Name the blood parasite species.
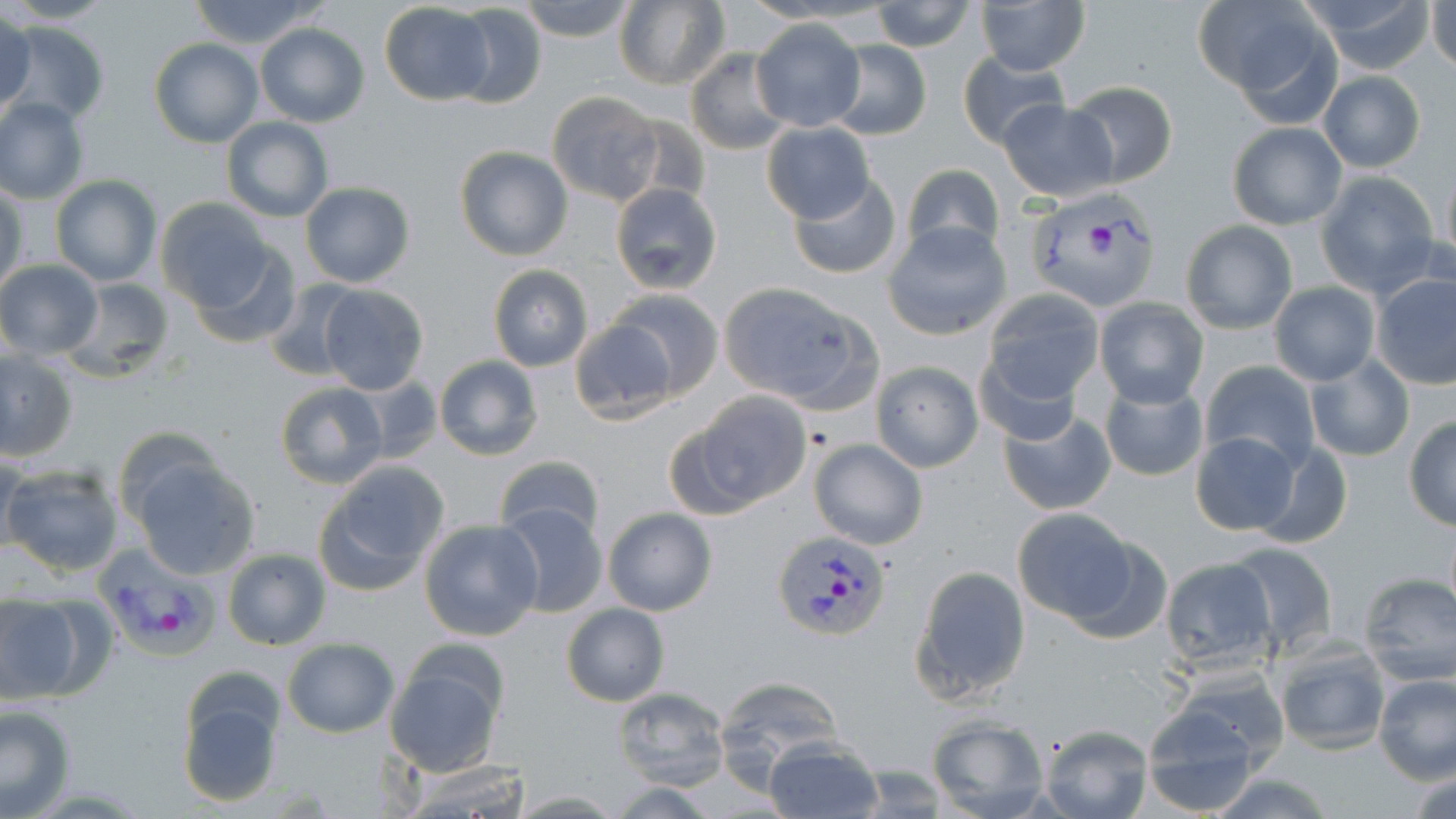
Plasmodium vivax.

{
  "uninfected_red_blood_cell_locations": "approximate bounding boxes as (x1,y1)-(x2,y2) corner pairs in pixels: (3,0)-(114,26), (186,0)-(327,47), (516,0)-(636,42), (738,0)-(888,27), (869,0)-(977,52), (1196,0)-(1339,111), (1299,0)-(1435,72), (1428,0)-(1456,74), (613,1)-(730,88), (975,2)-(1089,75), (379,3)-(494,105), (449,4)-(550,108), (0,12)-(37,119), (749,17)-(867,131), (5,20)-(108,126), (254,23)-(371,128), (150,37)-(262,147), (826,40)-(931,141), (686,50)-(790,155), (957,53)-(1069,150), (1317,71)-(1426,172), (1062,81)-(1179,187), (547,92)-(664,206), (0,97)-(88,203), (999,100)-(1117,200), (221,116)-(333,222), (761,121)-(877,223), (1226,122)-(1346,230), (453,146)-(573,261), (1439,158)-(1455,272), (899,163)-(1005,258), (1314,171)-(1442,298), (787,174)-(903,280), (50,175)-(161,287), (299,181)-(417,289), (610,182)-(723,294), (0,186)-(28,295), (155,196)-(274,310), (1179,219)-(1298,334), (883,222)-(1012,340), (187,241)-(303,349), (0,259)-(103,360), (487,265)-(593,371), (1370,270)-(1456,389), (61,277)-(176,382), (261,279)-(366,381), (1268,282)-(1379,385), (316,283)-(431,396), (720,283)-(857,408), (606,288)-(724,399), (980,289)-(1105,412), (1094,296)-(1210,409), (568,316)-(679,426), (0,347)-(80,462), (1305,353)-(1416,462), (433,355)-(544,460), (871,360)-(983,471), (1200,360)-(1320,475), (351,375)-(444,460), (1098,379)-(1209,482), (274,380)-(389,491), (672,394)-(813,517), (999,411)-(1117,516), (1403,415)-(1456,530), (1191,432)-(1301,538), (808,438)-(928,551), (1243,438)-(1353,547), (0,451)-(27,558), (128,454)-(261,581), (493,455)-(605,546), (314,462)-(447,595), (3,464)-(125,576), (498,500)-(606,618), (602,506)-(717,616), (1010,507)-(1139,625), (419,519)-(544,641), (1061,530)-(1176,643), (1224,541)-(1340,655), (221,547)-(331,650), (1159,558)-(1278,674), (910,565)-(1030,704), (1356,571)-(1456,685), (0,593)-(92,707), (561,604)-(668,707), (281,638)-(398,737), (1270,640)-(1393,755), (384,652)-(507,776), (1159,668)-(1292,774), (1373,673)-(1456,783), (175,674)-(286,809), (714,675)-(845,781), (613,685)-(730,792), (0,703)-(76,818), (1139,704)-(1269,816), (926,714)-(1052,817), (1038,724)-(1154,819), (762,738)-(882,818), (394,755)-(535,819), (1407,766)-(1456,819), (1203,769)-(1337,818), (609,781)-(722,816)",
  "field_of_view": "one of a larger specimen",
  "magnification": "1000x",
  "modality": "light microscopy",
  "preparation": "thin blood smear",
  "image_size": "1456×819 pixels",
  "stain": "May-Grünwald-Giemsa",
  "plasmodium_vivax_infected_red_blood_cell_locations": "approximate bounding boxes as (x1,y1)-(x2,y2) corner pairs in pixels: (1023,190)-(1163,310), (772,528)-(891,641), (91,544)-(218,659)"
}